Describe the morphology of the erythrocytes.
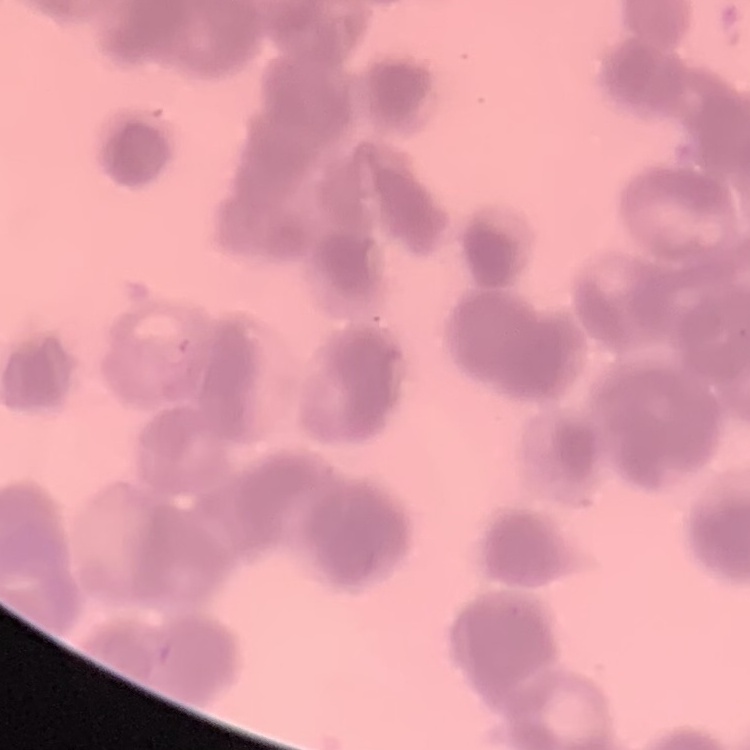
They show rouleaux formation.

Thin blood film. Stained with either Field's or Giemsa. Square crop of a larger photomicrograph.